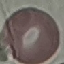
Malaria status: uninfected. Giemsa stain. Thin blood smear. Acquired by smartphone through the microscope eyepiece. Automatically extracted cell patch, resized to 64 × 64 pixels.